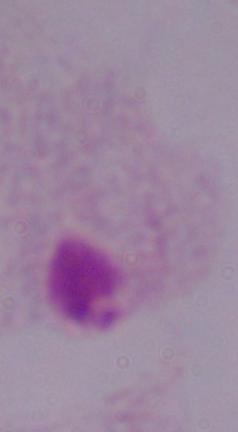
{
  "modality": "micrograph",
  "magnification": "1000x",
  "identification": "trichomonad"
}